Locate every blood parasite and identify its species.
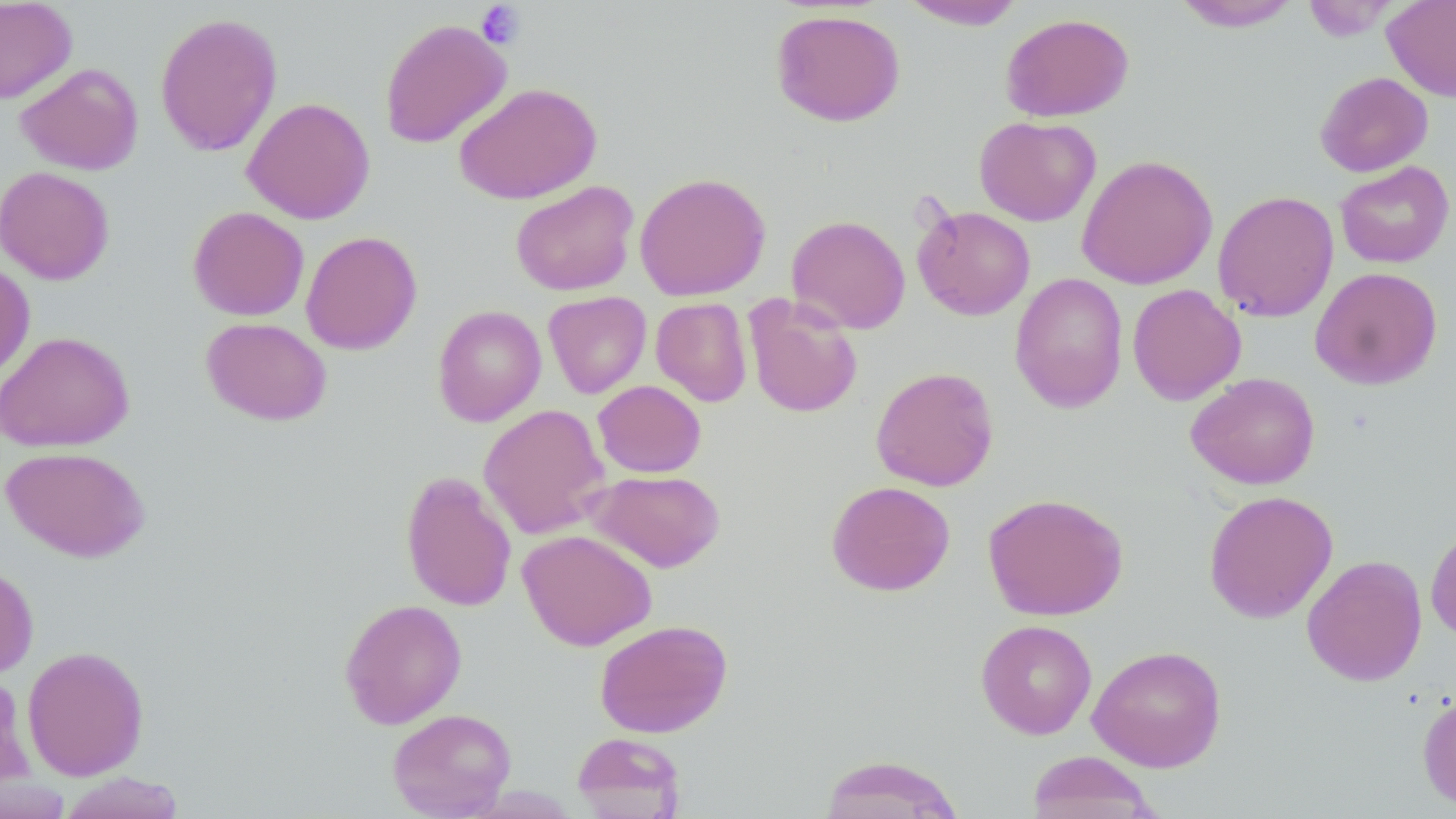

No blood parasites observed.

Summary:
  - Coordinate format: approximate bounding boxes as [x1, y1, x2, y2] in pixels
  - Uninfected red blood cell locations: [0, 0, 77, 104], [1382, 0, 1456, 102], [899, 1, 1027, 30], [1172, 1, 1301, 32], [1302, 1, 1398, 41], [770, 9, 905, 127], [155, 12, 283, 157], [1000, 12, 1135, 122], [379, 18, 512, 148], [15, 62, 144, 175], [1315, 71, 1433, 177], [453, 82, 602, 205], [241, 97, 376, 224], [974, 116, 1100, 226], [1076, 154, 1217, 290], [1335, 161, 1454, 269], [0, 166, 115, 285], [634, 172, 771, 301], [510, 180, 639, 297], [1212, 190, 1339, 322], [913, 204, 1036, 320], [188, 206, 309, 321], [786, 214, 911, 334], [301, 230, 422, 355], [0, 261, 35, 384], [1309, 267, 1443, 390], [1009, 272, 1129, 412], [1126, 284, 1246, 405], [543, 291, 651, 398], [743, 295, 863, 418], [651, 297, 752, 406], [432, 304, 546, 426], [200, 317, 332, 426], [0, 331, 135, 452], [871, 366, 999, 491], [1186, 372, 1321, 490], [592, 380, 706, 478], [478, 403, 610, 539], [1, 446, 151, 562], [585, 470, 726, 573], [400, 471, 518, 612], [826, 480, 956, 596], [1203, 490, 1338, 623], [983, 492, 1128, 620], [1425, 522, 1456, 646], [517, 529, 656, 650], [1301, 554, 1428, 687], [0, 562, 38, 680], [339, 598, 467, 729], [594, 619, 733, 738], [975, 619, 1098, 740], [22, 645, 149, 781], [1087, 645, 1227, 772], [1417, 691, 1456, 812], [387, 708, 516, 818], [571, 732, 687, 818], [1026, 751, 1161, 819], [817, 754, 966, 818], [58, 771, 188, 818]
  - Platelet locations: [475, 2, 526, 50]
  - Slide-level diagnosis: negative for blood parasites
  - Image size: 1456×819 pixels
  - Magnification: 1000x
  - Preparation: thin blood smear
  - Stain: May-Grünwald-Giemsa
  - Modality: optical microscopy
  - Field of view: one of a larger specimen